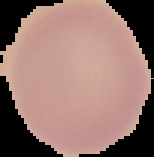

Malaria status: uninfected. Image is 154×157 pixels. From a thin blood smear. The area outside the segmented cell region is set to black.